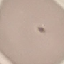

{
  "malaria_status": "uninfected",
  "preparation": "thin blood film",
  "image_type": "cell patch, automatically extracted from a larger field of view and resized to 64 × 64 pixels",
  "capture": "smartphone through the microscope eyepiece",
  "stain": "Giemsa"
}